Classify this cell by malaria status.
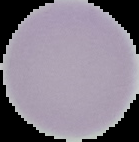
It is uninfected.

Image is 139×142 pixels. Segmented cell region on a black background. From a thin blood film.